State the preparation type.
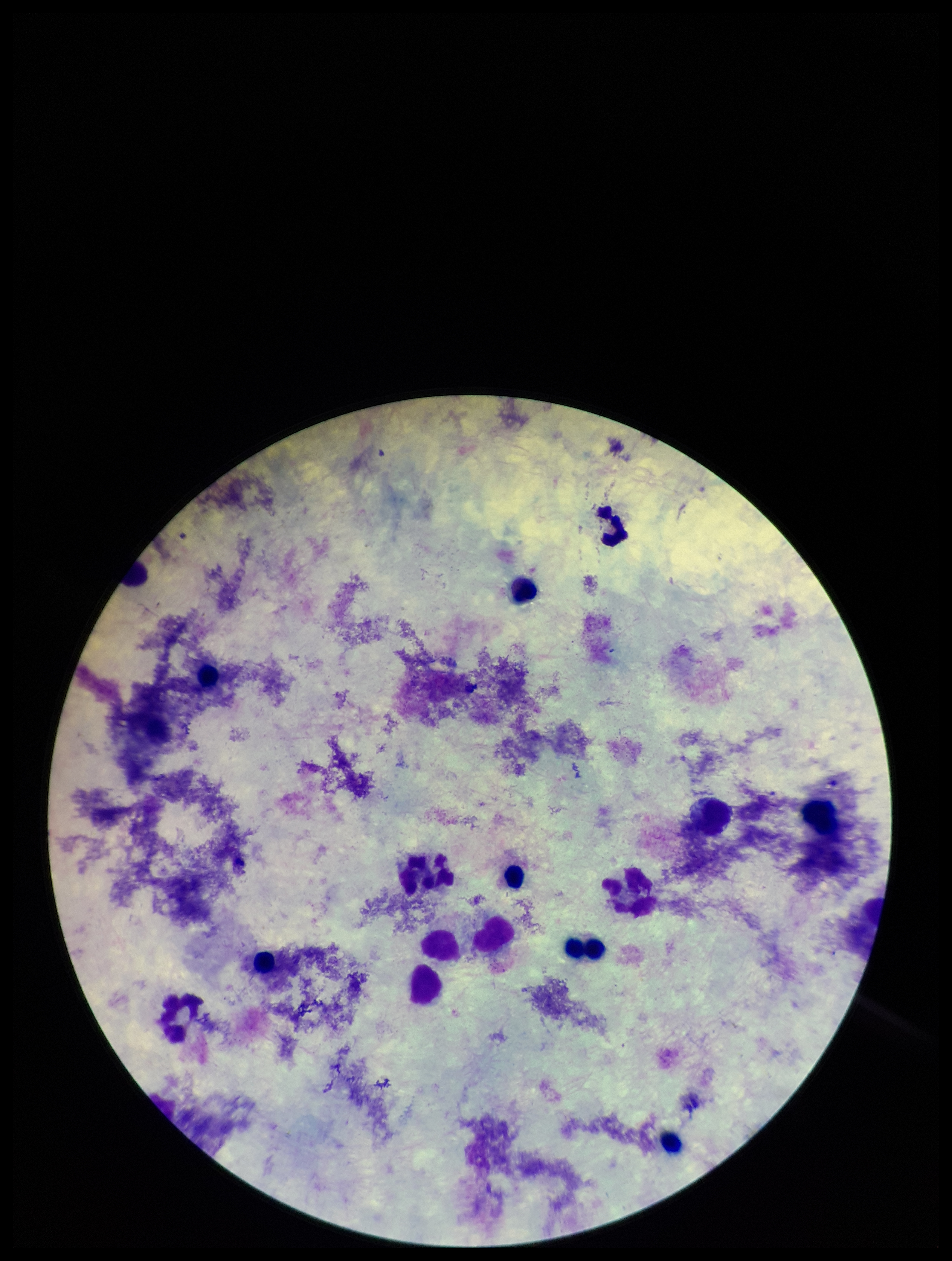

A thick smear.

Summary:
  - Field of view: single
  - Leukocyte count: 14
  - Plasmodium parasites: none seen
  - Patient malaria status: negative
  - Image size: 952×1261 pixels
  - Stain: Giemsa
  - Capture: smartphone photograph through the microscope eyepiece
  - Parasite count: 0